Assess this cell for malaria.
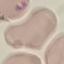
Uninfected.

Summary:
  - Stain: Giemsa
  - Capture: smartphone camera at the microscope eyepiece
  - Image type: cell patch, automatically extracted from a larger field of view and resized to 64 × 64 pixels
  - Preparation: thin smear